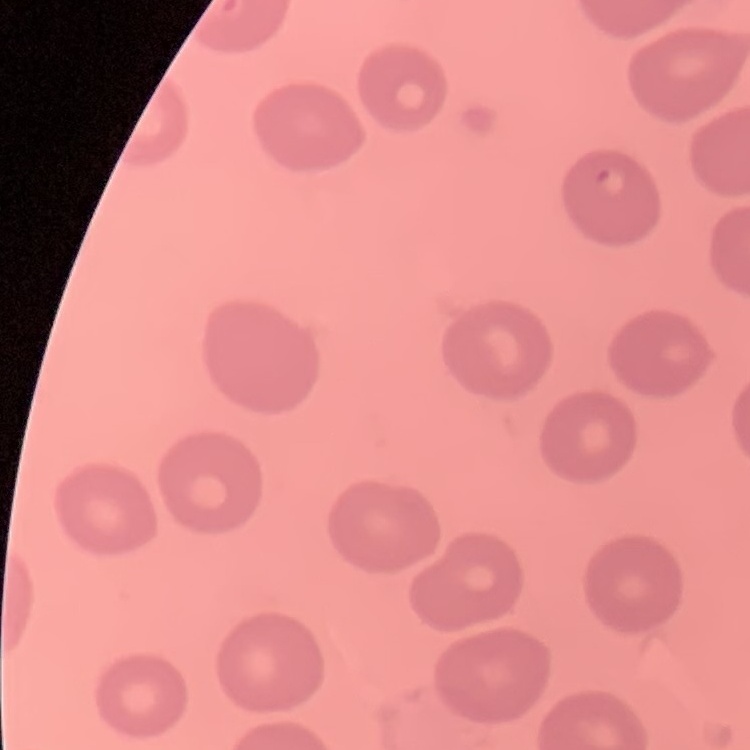
Summary:
  - Red blood cell morphology: no rouleaux formation
  - Image type: one tile cut from a larger photomicrograph
  - Preparation: thin peripheral smear
  - Stain: Field's or Giemsa